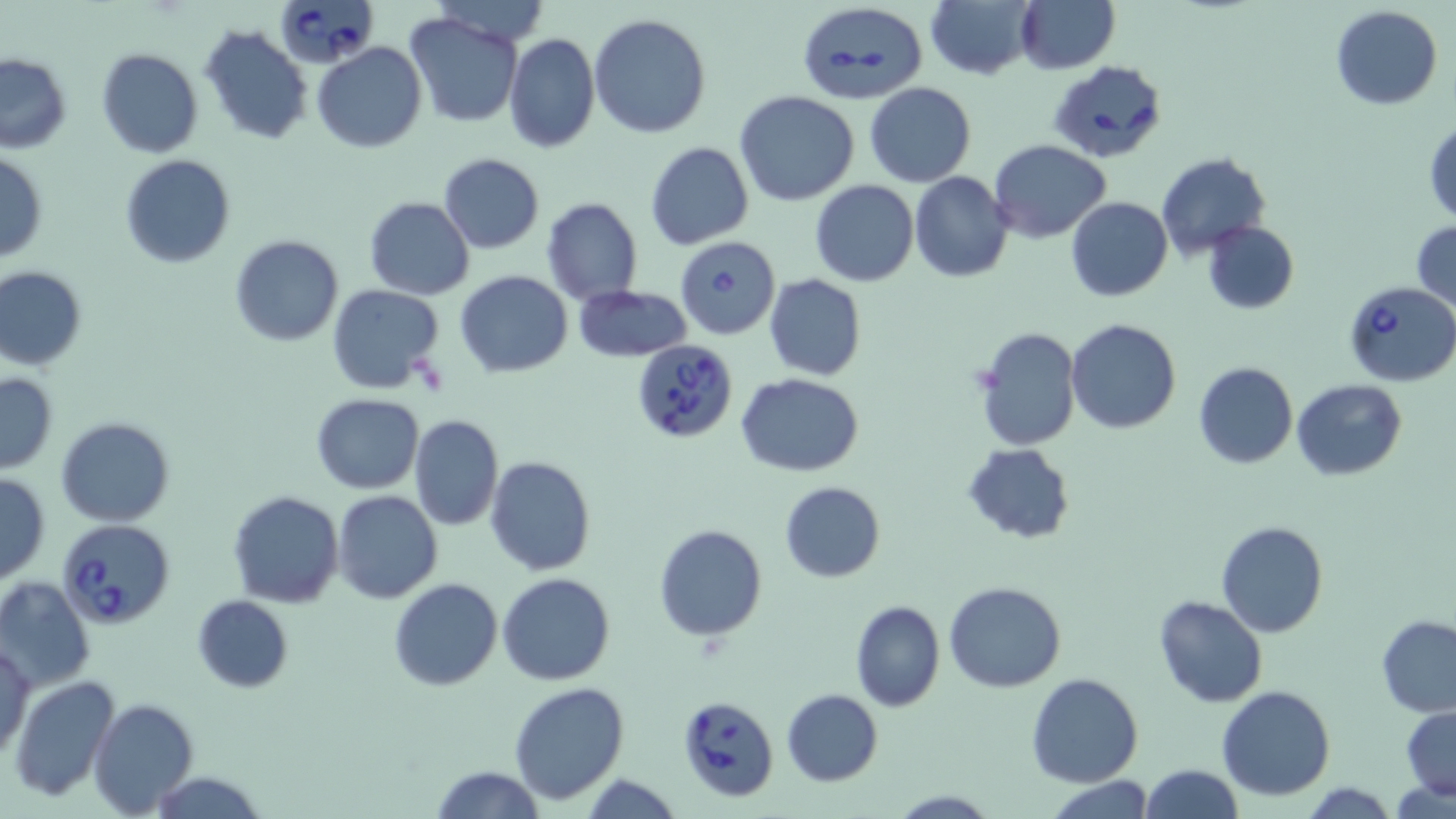 Approximate bounding boxes as [x1, y1, x2, y2] in pixels. Babesia divergens-infected red blood cell locations: [275, 0, 378, 68], [796, 0, 926, 105], [1048, 59, 1165, 165], [675, 236, 779, 339], [1344, 281, 1456, 385], [631, 340, 738, 443], [57, 518, 176, 631], [675, 694, 780, 800]. Uninfected red blood cell locations: [926, 0, 1038, 79], [1016, 1, 1119, 74], [1331, 6, 1442, 111], [406, 11, 524, 127], [588, 13, 711, 139], [199, 25, 313, 146], [505, 33, 599, 153], [313, 43, 426, 152], [96, 48, 202, 158], [0, 54, 71, 153], [864, 83, 975, 187], [734, 91, 858, 207], [1425, 118, 1456, 224], [990, 140, 1110, 242], [645, 142, 753, 250], [0, 152, 47, 262], [1156, 152, 1269, 260], [438, 153, 545, 254], [120, 155, 235, 269], [908, 172, 1014, 282], [811, 181, 919, 287], [347, 196, 458, 391], [364, 196, 474, 299], [1067, 197, 1172, 302], [542, 199, 643, 304], [1202, 221, 1298, 314], [1411, 221, 1455, 312], [229, 235, 343, 347], [0, 265, 88, 372], [455, 271, 572, 377], [764, 273, 866, 382], [326, 283, 445, 393], [572, 284, 691, 362], [1066, 320, 1181, 435], [974, 327, 1081, 450], [1194, 362, 1297, 469], [0, 372, 59, 474], [736, 373, 865, 475], [1293, 379, 1406, 480], [312, 394, 425, 493], [410, 415, 504, 531], [57, 416, 176, 526], [962, 443, 1075, 544], [485, 455, 595, 575], [0, 473, 49, 586], [779, 483, 886, 583], [227, 490, 343, 609], [332, 490, 443, 605], [1215, 521, 1328, 637], [653, 523, 768, 642], [498, 573, 616, 686], [0, 577, 95, 692], [389, 578, 502, 691], [944, 581, 1068, 693], [192, 594, 293, 692], [1154, 595, 1268, 708], [849, 600, 946, 712], [1377, 615, 1456, 717], [1, 638, 34, 759], [1026, 672, 1143, 787], [10, 675, 121, 803], [509, 682, 630, 804], [1216, 685, 1336, 801], [781, 688, 882, 786], [88, 699, 197, 816], [1400, 704, 1456, 800], [1138, 764, 1243, 819], [430, 765, 543, 819], [149, 772, 268, 818], [578, 774, 686, 817], [1046, 775, 1156, 819]. Slide-level diagnosis: Babesia divergens. Captured at 1000x magnification. One field of a larger specimen. Thin blood smear. May-Grünwald-Giemsa-stained preparation. Optical microscopy. Image is 1456×819 pixels.